Comment on the morphology of the red blood cells.
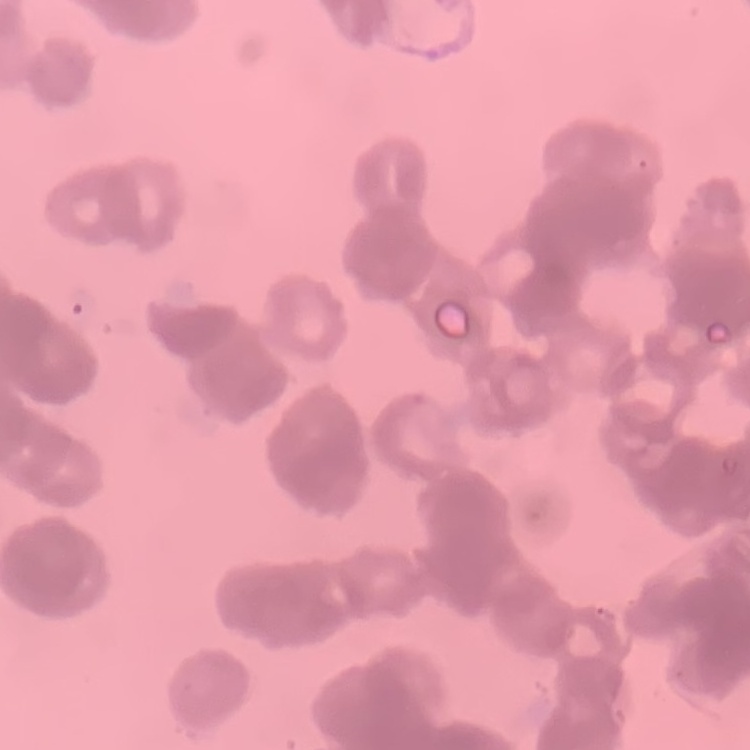

They show rouleaux formation.

image type = one tile cut from a larger photomicrograph
preparation = thin blood smear
stain = Field's or Giemsa